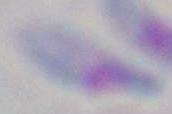 Toxoplasma gondii is seen. Micrograph. Captured at 1000x magnification.